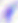

Toxoplasma gondii is shown. Micrograph. Captured at 400x magnification.